Evaluate for parasitized red blood cells.
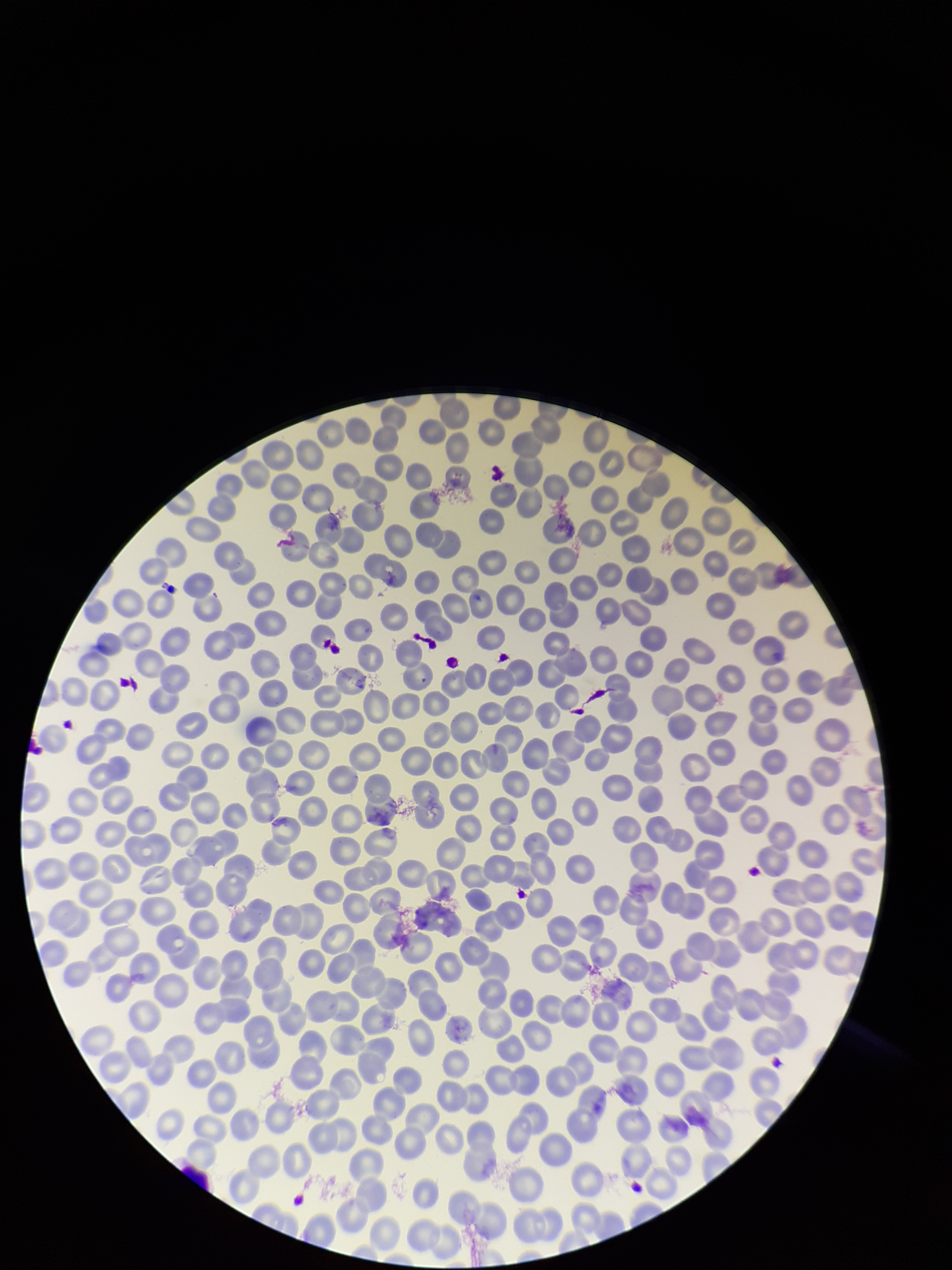
None detected.

image size = 952×1270 pixels
stain = Giemsa
field of view = single
parasitized red blood cell count = 0
preparation = thin smear
red blood cell count = 350
patient malaria status = positive
species reported for this patient = Plasmodium falciparum
capture = smartphone photograph through the microscope eyepiece